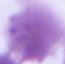

modality = micrograph
magnification = 1000x
identification = erythrocyte